Outline every leukocyte.
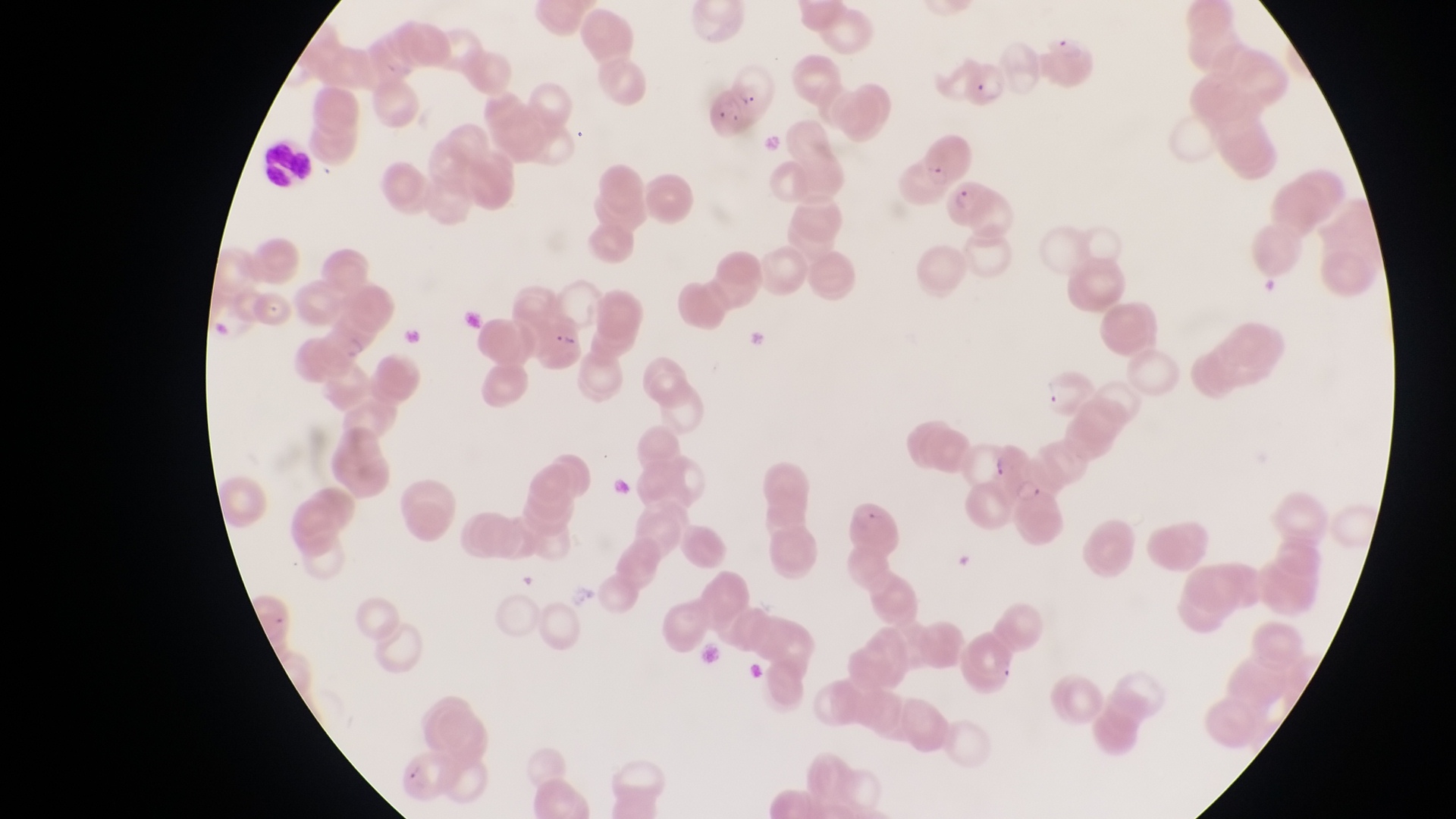

Approximate bounding boxes as (left, top, right, bottom) in pixels.
Leukocytes: (257, 140, 315, 186).

parasitised red blood cell locations = approximate bounding boxes as (left, top, right, bottom) in pixels: (951, 61, 1010, 106), (721, 66, 780, 119), (946, 182, 1010, 241), (320, 318, 375, 368), (1010, 468, 1071, 547)
magnification = 1000x
image size = 1456×819 pixels
capture = smartphone photograph through the eyepiece of an Olympus CX-23 microscope
country = Uganda
field of view = single
artifact (platelet-like body, stain precipitate, or debris) locations = approximate bounding boxes as (left, top, right, bottom) in pixels: (551, 325, 583, 357)
preparation = thin blood smear